Report the malaria status of this cell.
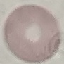
It is uninfected.

preparation = thin blood smear
capture = smartphone camera at the microscope eyepiece
image type = automatically extracted cell patch, resized to 64 × 64 pixels
stain = Giemsa